Assess this cell for malaria.
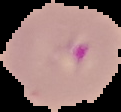

It is parasitized.

From a thin blood film. The area outside the segmented cell region is set to black. Image is 121×112 pixels.